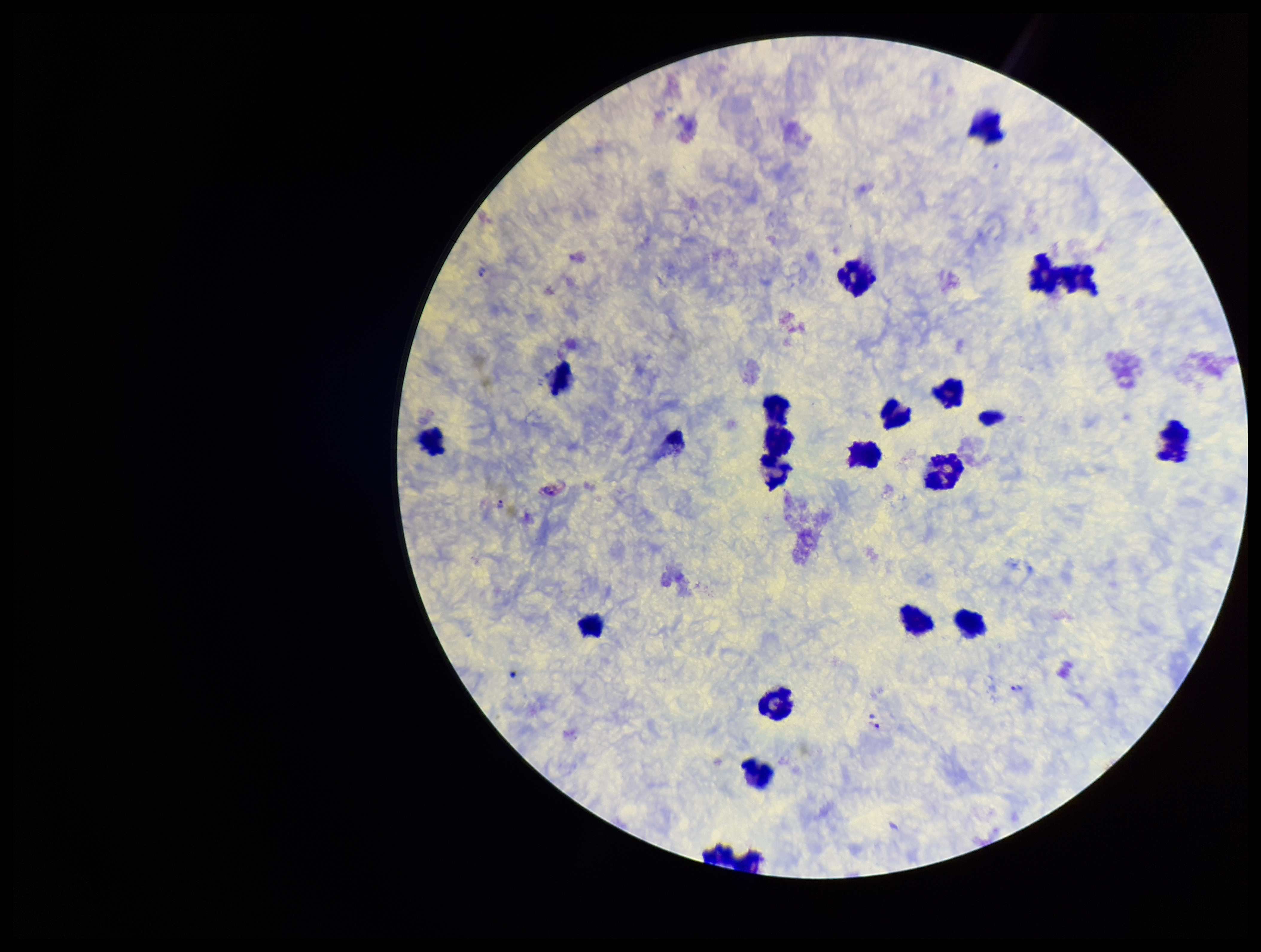
Species reported for this patient: Plasmodium vivax. Leukocyte count: 20. Parasite count: 4. One field from this slide. Smartphone photograph taken through the eyepiece of a microscope. Preparation: thick. Patient malaria status: positive. Image is 1261×952 pixels. Plasmodium parasites: identified. Stained with Giemsa.